Report the malaria status.
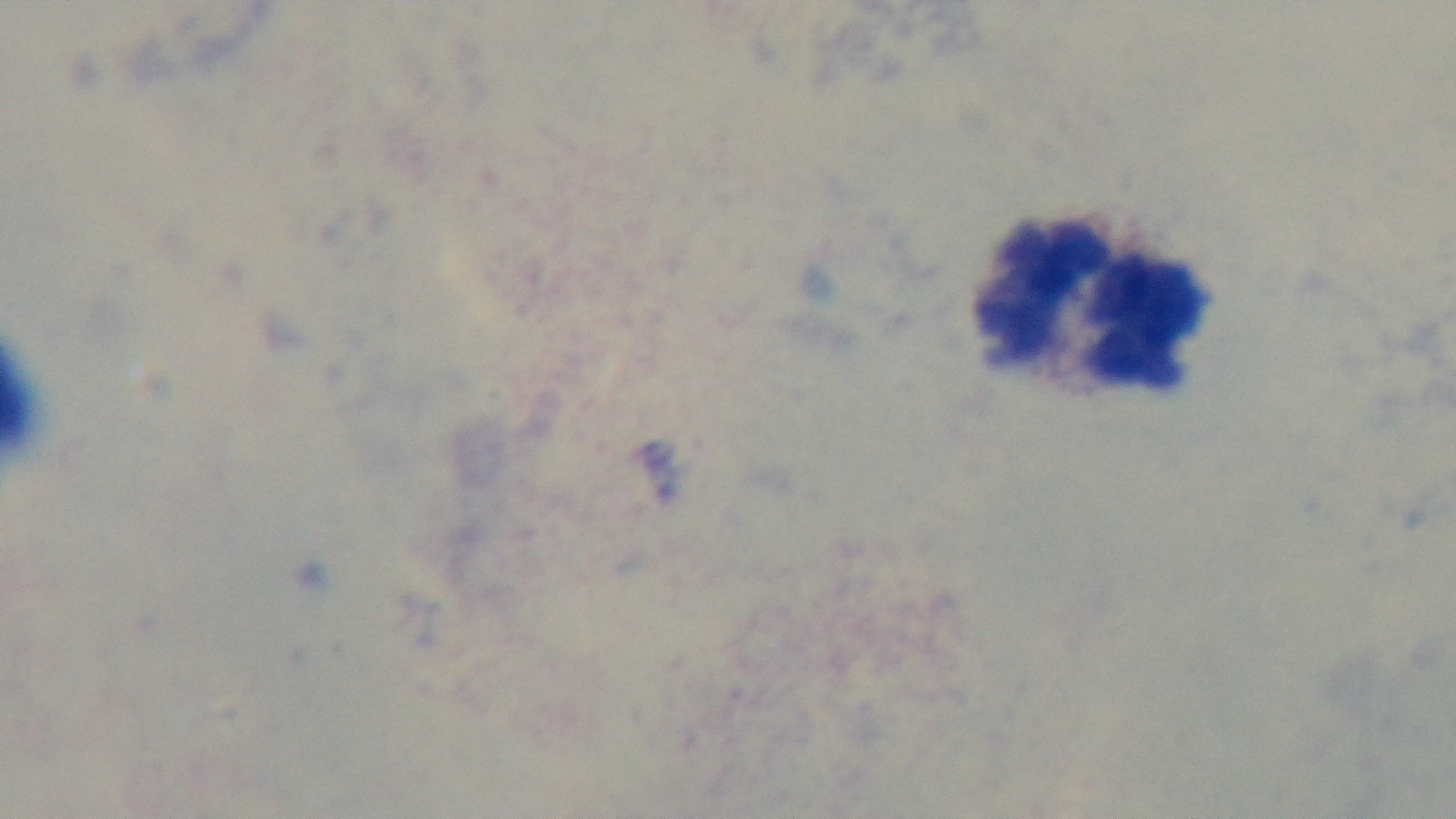
It is uninfected.

Summary:
  - Field of view: single
  - Objective: 100x oil immersion
  - Capture: mounted 4K digital camera
  - Stain: Giemsa
  - Modality: light microscopy
  - Preparation: thick blood film